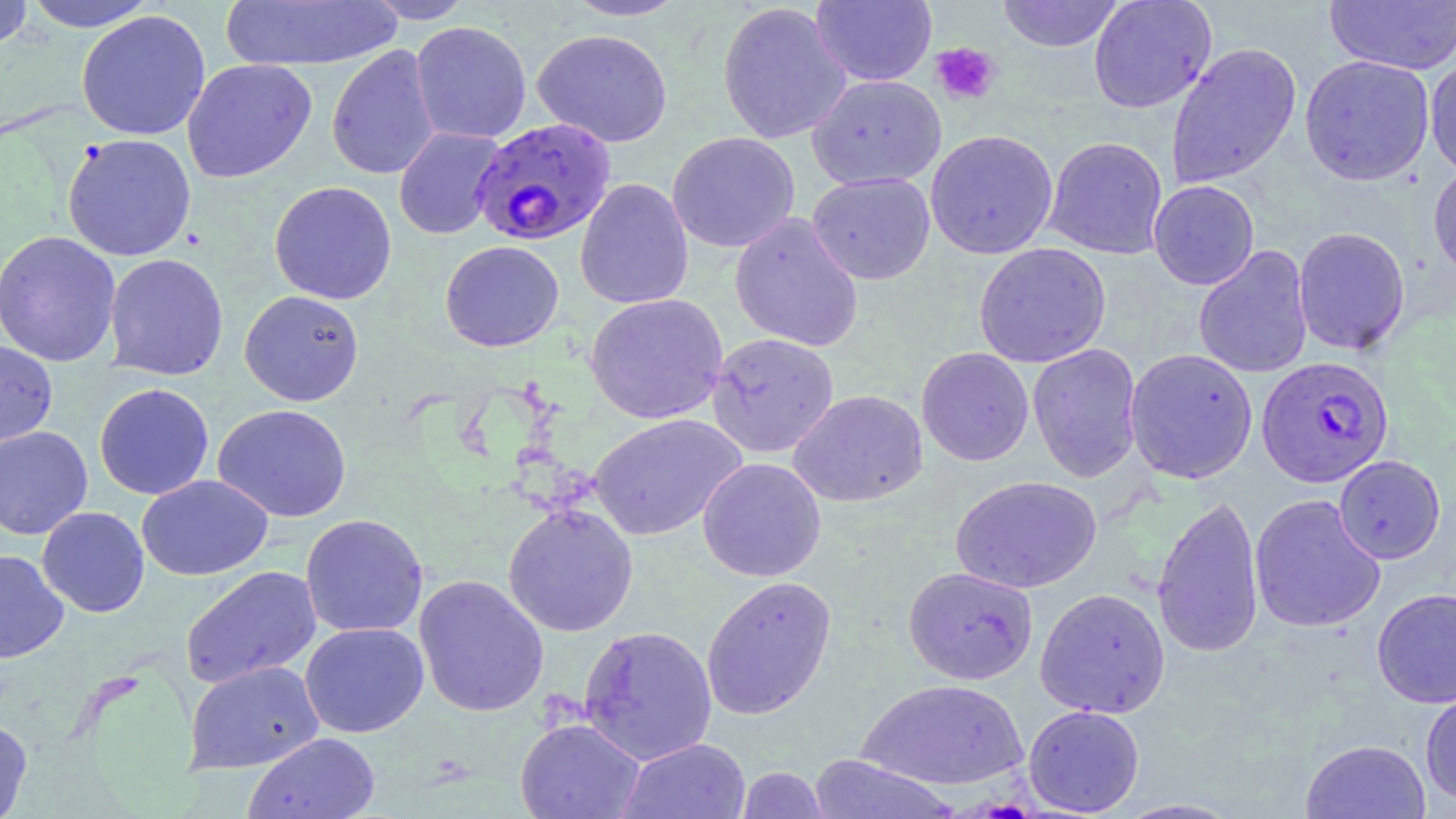
slide-level diagnosis = Plasmodium falciparum
magnification = 1000x
modality = optical microscopy
Plasmodium falciparum-infected red blood cell locations = approximate bounding boxes as [x1, y1, x2, y2] in pixels: [471, 117, 617, 247], [1257, 356, 1394, 487]
field of view = single
uninfected red blood cell locations = approximate bounding boxes as [x1, y1, x2, y2] in pixels: [20, 0, 161, 32], [363, 0, 477, 24], [561, 0, 691, 22], [810, 0, 937, 87], [997, 0, 1124, 52], [1088, 0, 1217, 114], [220, 1, 404, 71], [716, 1, 852, 145], [1323, 1, 1456, 75], [0, 2, 35, 52], [75, 10, 211, 141], [410, 21, 532, 144], [531, 28, 674, 148], [1166, 42, 1302, 188], [326, 44, 441, 181], [1299, 54, 1435, 186], [1425, 56, 1456, 181], [182, 59, 317, 183], [806, 73, 947, 190], [393, 126, 505, 240], [925, 129, 1059, 259], [667, 131, 801, 253], [62, 133, 197, 261], [1044, 136, 1168, 259], [1428, 162, 1456, 283], [806, 172, 936, 285], [575, 178, 694, 310], [1148, 180, 1260, 290], [269, 181, 397, 305], [729, 212, 864, 353], [1293, 226, 1411, 356], [0, 230, 122, 367], [440, 240, 564, 353], [973, 242, 1111, 368], [1193, 245, 1314, 379], [104, 253, 229, 381], [239, 290, 365, 406], [585, 293, 728, 425], [707, 332, 839, 458], [0, 339, 58, 450], [1027, 343, 1143, 483], [916, 347, 1034, 466], [1124, 348, 1258, 484], [94, 383, 215, 500], [787, 389, 928, 508], [213, 403, 352, 522], [587, 413, 747, 541], [0, 426, 93, 540], [1334, 455, 1446, 564], [697, 457, 826, 582], [137, 474, 273, 581], [950, 475, 1102, 594], [1152, 493, 1264, 660], [1249, 493, 1386, 633], [502, 502, 639, 638], [37, 506, 150, 617], [300, 513, 429, 638], [0, 549, 69, 663], [179, 565, 323, 689], [903, 566, 1038, 685], [413, 574, 549, 718], [701, 575, 837, 720], [1034, 587, 1171, 718], [1371, 587, 1456, 708], [299, 622, 429, 738], [578, 625, 718, 764], [183, 660, 325, 774], [857, 678, 1028, 791], [1420, 688, 1456, 807], [1023, 704, 1145, 816], [0, 716, 32, 819], [514, 718, 645, 819], [243, 732, 381, 819], [617, 738, 752, 819], [1300, 739, 1431, 819], [807, 754, 961, 819], [735, 766, 830, 818], [1112, 798, 1246, 818]
platelet locations = approximate bounding boxes as [x1, y1, x2, y2] in pixels: [930, 42, 1001, 106]
image size = 1456×819 pixels
preparation = thin blood smear
stain = May-Grünwald-Giemsa